Describe the morphology of the erythrocytes.
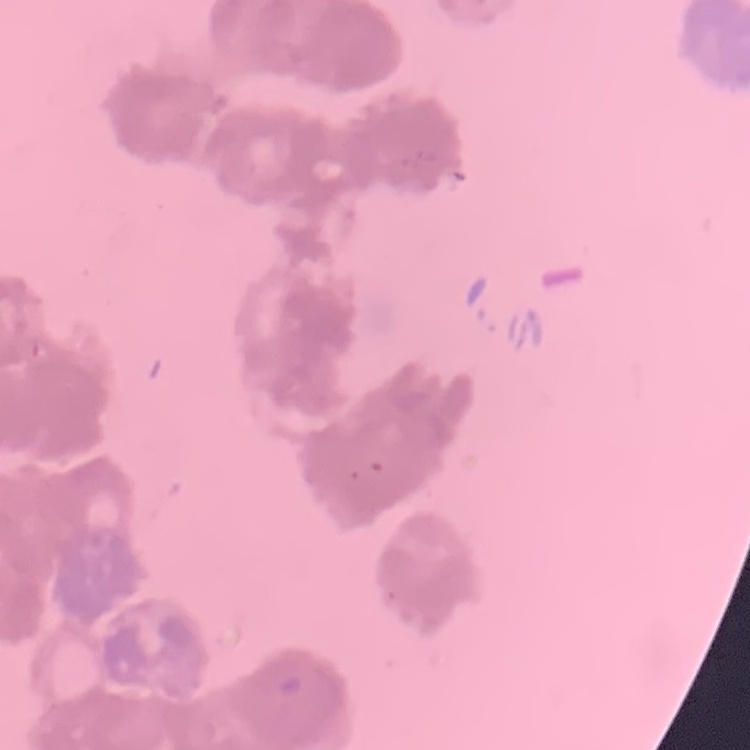
Rouleaux formation.

Summary:
  - Stain: Field's or Giemsa
  - Image type: one tile cut from a larger photomicrograph
  - Preparation: thin blood smear